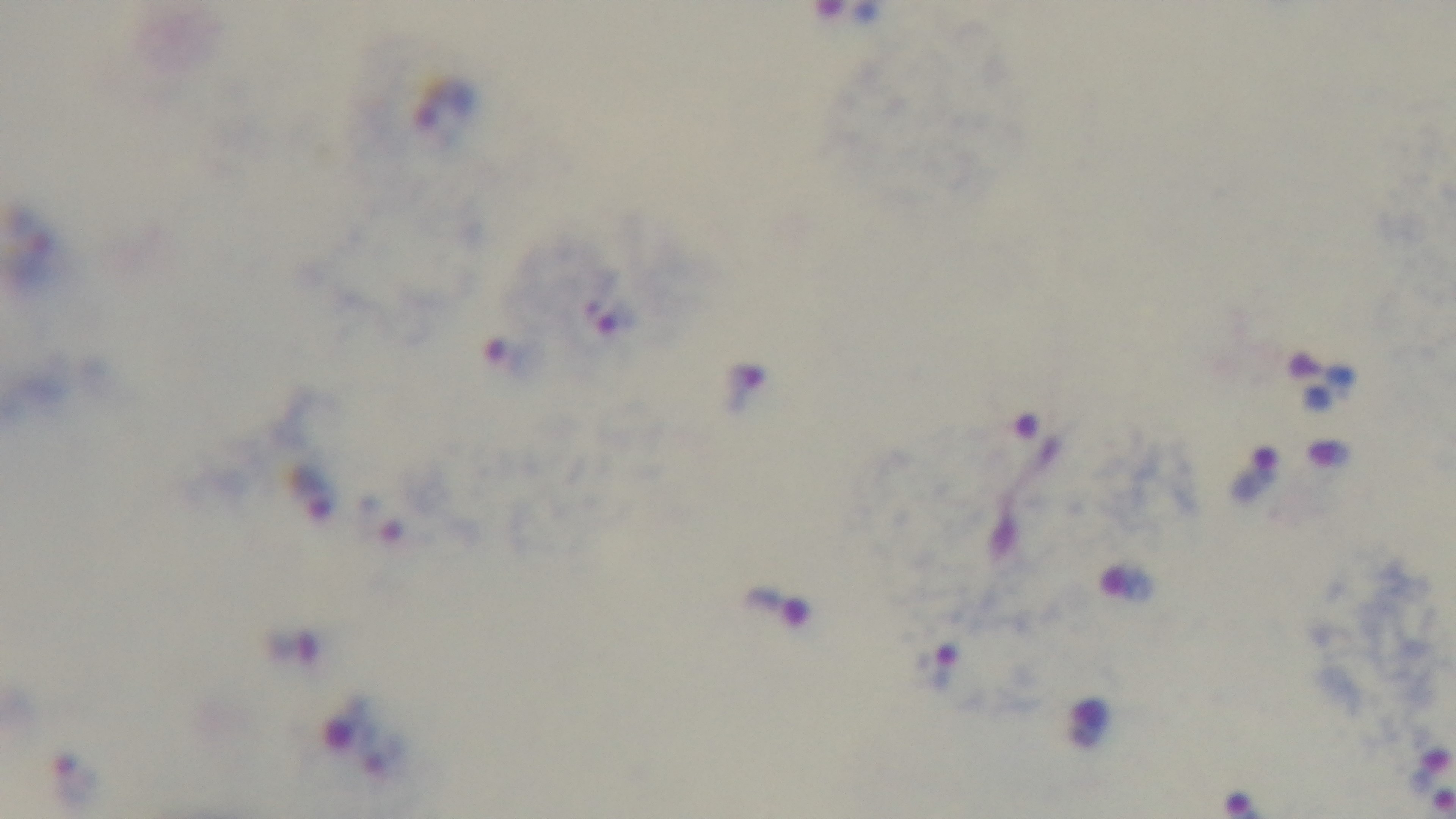
Summary:
  - Field of view: single
  - Modality: light microscopy
  - Capture: mounted 4K digital camera
  - Objective: 100x oil immersion
  - Preparation: thick blood film
  - Stain: Giemsa
  - Malaria status: infected